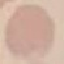
Result: no malaria parasites detected. Automatically extracted cell patch, resized to 64 × 64 pixels. Giemsa stain. Photographed with a smartphone camera at the microscope eyepiece. Thin blood smear.